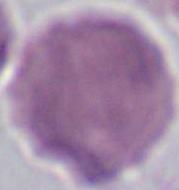

identification = red blood cell
modality = micrograph
magnification = 1000x